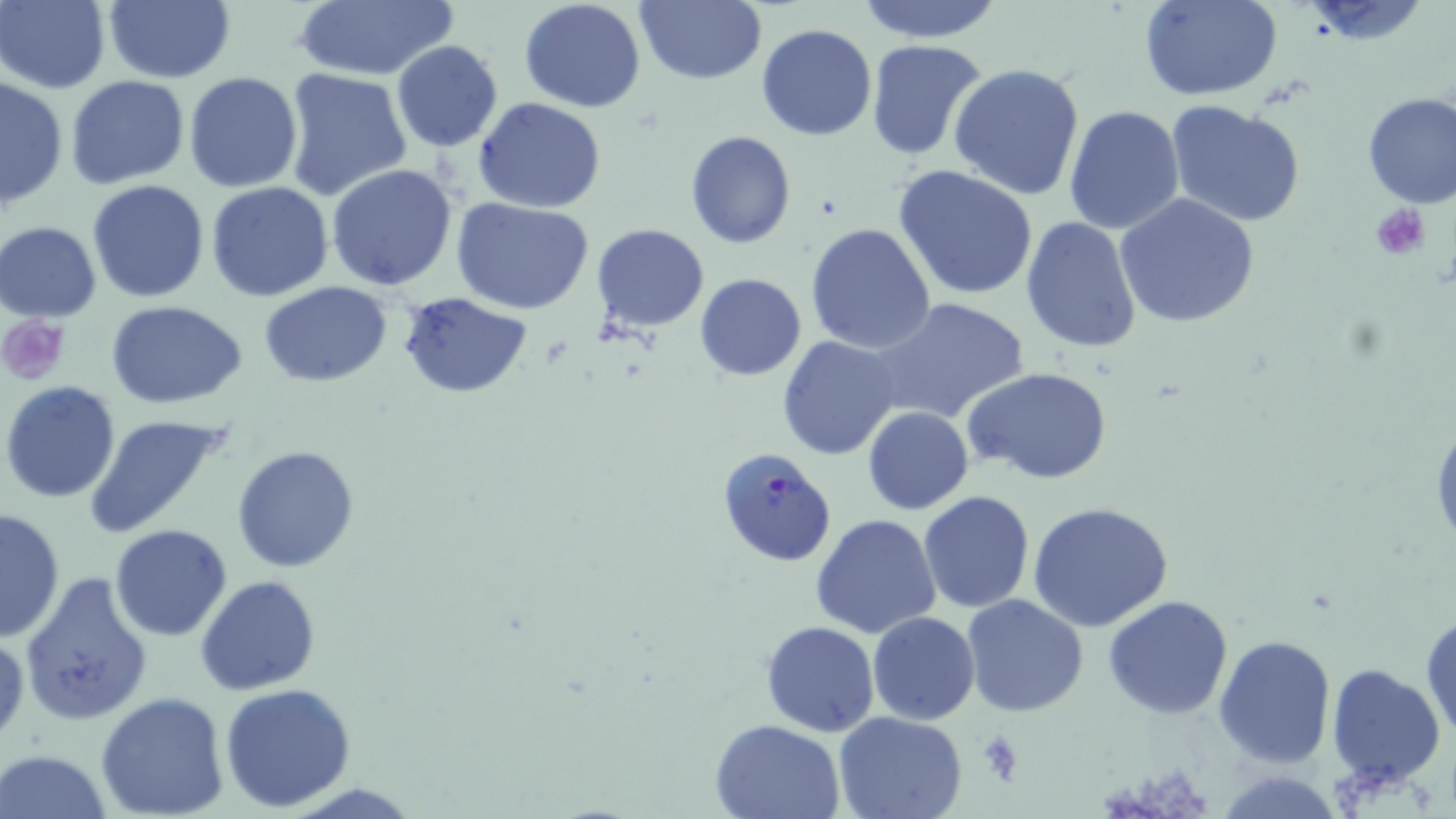
Summary:
  - Coordinate format: approximate bounding boxes as named x1/y1/x2/y2 corners in pixels
  - Platelet locations: (x1=1370, y1=202, x2=1431, y2=260), (x1=3, y1=315, x2=73, y2=385), (x1=978, y1=731, x2=1026, y2=782)
  - Uninfected red blood cell locations: (x1=0, y1=0, x2=110, y2=92), (x1=102, y1=0, x2=236, y2=84), (x1=636, y1=0, x2=767, y2=85), (x1=856, y1=0, x2=1004, y2=42), (x1=1140, y1=0, x2=1283, y2=100), (x1=292, y1=1, x2=456, y2=82), (x1=518, y1=1, x2=646, y2=113), (x1=756, y1=23, x2=877, y2=140), (x1=865, y1=38, x2=988, y2=162), (x1=390, y1=40, x2=503, y2=152), (x1=948, y1=63, x2=1085, y2=202), (x1=281, y1=69, x2=410, y2=202), (x1=184, y1=72, x2=303, y2=192), (x1=66, y1=75, x2=190, y2=190), (x1=0, y1=76, x2=67, y2=211), (x1=1360, y1=90, x2=1456, y2=208), (x1=472, y1=97, x2=606, y2=214), (x1=1165, y1=100, x2=1308, y2=229), (x1=1064, y1=105, x2=1185, y2=233), (x1=685, y1=131, x2=796, y2=248), (x1=325, y1=164, x2=458, y2=290), (x1=893, y1=164, x2=1038, y2=301), (x1=87, y1=179, x2=211, y2=303), (x1=206, y1=182, x2=333, y2=301), (x1=1114, y1=194, x2=1260, y2=327), (x1=453, y1=199, x2=594, y2=315), (x1=1021, y1=218, x2=1143, y2=355), (x1=1, y1=220, x2=101, y2=321), (x1=804, y1=223, x2=937, y2=355), (x1=591, y1=224, x2=709, y2=331), (x1=695, y1=273, x2=806, y2=381), (x1=259, y1=281, x2=392, y2=386), (x1=397, y1=292, x2=532, y2=398), (x1=870, y1=297, x2=1029, y2=425), (x1=105, y1=301, x2=248, y2=408), (x1=777, y1=335, x2=903, y2=461), (x1=963, y1=365, x2=1114, y2=486), (x1=1, y1=382, x2=121, y2=503), (x1=861, y1=407, x2=973, y2=515), (x1=1430, y1=409, x2=1456, y2=560), (x1=81, y1=412, x2=234, y2=539), (x1=232, y1=445, x2=361, y2=574), (x1=918, y1=490, x2=1034, y2=612), (x1=1027, y1=501, x2=1173, y2=631), (x1=1, y1=506, x2=66, y2=643), (x1=811, y1=514, x2=942, y2=640), (x1=109, y1=524, x2=232, y2=642), (x1=20, y1=571, x2=154, y2=727), (x1=196, y1=574, x2=322, y2=696), (x1=960, y1=594, x2=1089, y2=718), (x1=1103, y1=594, x2=1234, y2=719), (x1=1421, y1=608, x2=1455, y2=744), (x1=866, y1=612, x2=980, y2=726), (x1=760, y1=620, x2=881, y2=737), (x1=0, y1=631, x2=27, y2=747), (x1=1213, y1=633, x2=1336, y2=768), (x1=1326, y1=662, x2=1445, y2=788), (x1=220, y1=683, x2=357, y2=813), (x1=95, y1=691, x2=230, y2=819), (x1=834, y1=710, x2=968, y2=819), (x1=709, y1=718, x2=845, y2=818), (x1=1, y1=750, x2=115, y2=819), (x1=1213, y1=767, x2=1345, y2=818)
  - Plasmodium falciparum-infected red blood cell locations: (x1=715, y1=446, x2=837, y2=566)
  - Slide-level diagnosis: Plasmodium falciparum
  - Preparation: thin blood smear
  - Field of view: one of a larger specimen
  - Image size: 1456×819 pixels
  - Modality: optical microscopy
  - Stain: May-Grünwald-Giemsa
  - Magnification: 1000x